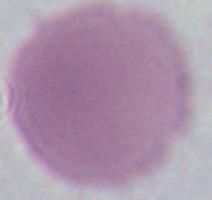

Summary:
  - Magnification: 1000x
  - Identification: erythrocyte
  - Modality: micrograph